Identify the blood parasite species.
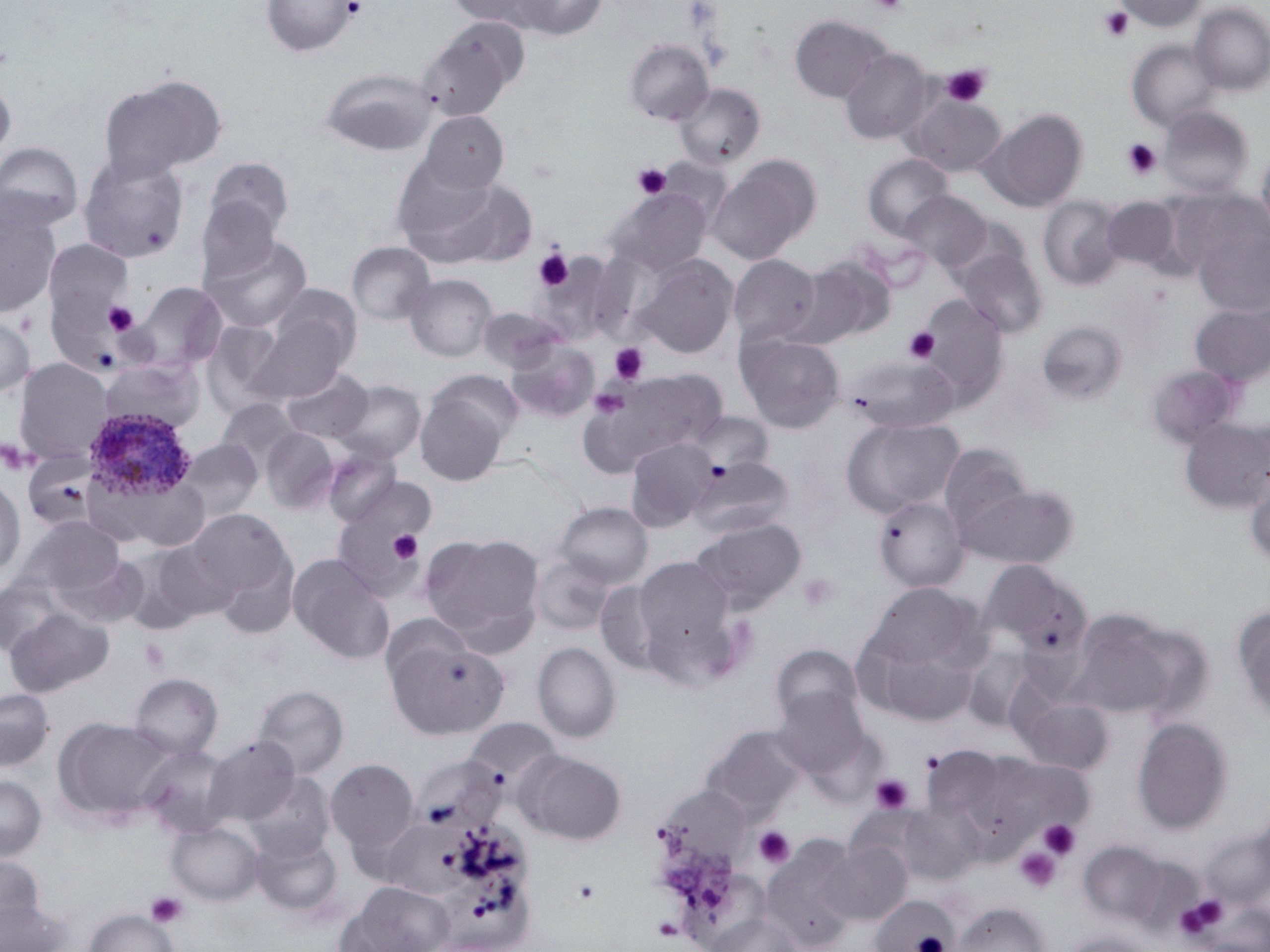
Plasmodium ovale.

{
  "modality": "optical microscopy",
  "platelet_locations": "approximate bounding boxes as (x1, y1, x2, y2) in pixels: (343, 0, 367, 19), (867, 0, 910, 14), (1097, 6, 1133, 43), (942, 64, 991, 108), (1121, 138, 1162, 179), (632, 162, 672, 200), (534, 248, 574, 291), (104, 301, 139, 336), (903, 326, 940, 364), (609, 342, 649, 384), (589, 387, 629, 419), (390, 531, 424, 563), (798, 572, 839, 613), (140, 639, 170, 672), (920, 751, 945, 774), (869, 774, 914, 815), (1039, 820, 1080, 859), (754, 826, 795, 869), (1014, 847, 1062, 893), (572, 877, 601, 905), (145, 891, 189, 928), (1178, 896, 1229, 936)",
  "field_of_view": "one of a larger specimen",
  "image_size": "1270×952 pixels",
  "uninfected_red_blood_cell_locations": "approximate bounding boxes as (x1, y1, x2, y2) in pixels: (260, 0, 360, 56), (510, 0, 607, 40), (1115, 0, 1206, 32), (445, 1, 551, 29), (1189, 2, 1270, 96), (788, 14, 892, 103), (419, 19, 529, 119), (624, 39, 714, 125), (1127, 39, 1220, 132), (838, 48, 933, 145), (320, 68, 437, 155), (98, 74, 226, 181), (0, 77, 16, 165), (673, 83, 765, 170), (903, 92, 1007, 176), (1158, 106, 1253, 197), (979, 108, 1088, 212), (418, 111, 509, 195), (0, 141, 84, 231), (1256, 149, 1270, 246), (78, 154, 189, 263), (862, 154, 954, 240), (707, 155, 821, 264), (202, 157, 294, 247), (391, 160, 525, 265), (606, 187, 713, 277), (195, 190, 286, 286), (898, 190, 992, 273), (1038, 196, 1125, 291), (1101, 196, 1180, 270), (0, 199, 61, 319), (1194, 226, 1270, 317), (203, 235, 312, 333), (44, 239, 134, 327), (347, 242, 435, 325), (953, 244, 1048, 338), (728, 254, 821, 346), (636, 255, 738, 358), (793, 255, 895, 346), (44, 270, 140, 380), (404, 274, 497, 361), (132, 282, 228, 373), (913, 294, 1009, 410), (244, 295, 359, 402), (1189, 303, 1270, 387), (477, 307, 566, 373), (0, 311, 36, 399), (1036, 319, 1129, 405), (203, 320, 290, 415), (736, 331, 846, 433), (505, 339, 599, 421), (849, 356, 958, 433), (13, 358, 114, 464), (1146, 364, 1242, 449), (281, 367, 374, 444), (99, 368, 203, 443), (587, 368, 729, 467), (333, 380, 426, 463), (414, 383, 512, 486), (216, 398, 301, 476), (1179, 417, 1270, 513), (842, 418, 964, 515), (260, 427, 340, 513), (625, 437, 717, 531), (179, 439, 263, 521), (939, 444, 1034, 537), (322, 445, 403, 526), (22, 452, 99, 532), (689, 455, 794, 538), (1244, 471, 1270, 568), (92, 472, 209, 553), (330, 474, 434, 599), (0, 477, 26, 579), (954, 482, 1079, 569), (872, 497, 967, 593), (553, 501, 653, 589), (184, 508, 295, 615), (13, 516, 127, 606), (691, 517, 806, 614), (419, 532, 545, 651), (208, 544, 301, 640), (114, 546, 204, 634), (55, 552, 148, 628), (287, 553, 394, 665), (531, 553, 617, 636), (629, 555, 739, 670), (979, 559, 1093, 661), (0, 578, 68, 657), (595, 579, 671, 676), (853, 585, 990, 724), (4, 606, 114, 697), (1233, 607, 1270, 723), (1066, 610, 1179, 720), (380, 613, 473, 690), (386, 637, 510, 739), (531, 642, 622, 743), (771, 644, 863, 728), (962, 646, 1039, 732), (129, 673, 223, 760), (253, 685, 349, 778), (772, 687, 873, 783), (0, 688, 54, 772), (1017, 695, 1113, 774), (52, 716, 175, 826), (1132, 717, 1233, 835), (464, 718, 562, 786), (701, 725, 807, 822), (204, 734, 301, 826), (139, 744, 234, 838), (517, 750, 626, 845), (325, 758, 419, 856), (415, 758, 510, 832), (243, 773, 335, 862), (0, 775, 47, 861), (654, 786, 753, 872), (897, 802, 985, 885), (166, 821, 264, 906), (391, 823, 472, 900), (1201, 831, 1269, 909), (250, 832, 342, 916), (759, 836, 861, 950), (820, 840, 911, 924), (1079, 841, 1169, 926), (0, 853, 45, 935), (340, 881, 455, 952), (870, 896, 958, 951), (0, 897, 68, 952), (954, 902, 1051, 952), (82, 908, 179, 952), (709, 913, 803, 952), (1063, 931, 1157, 952)",
  "magnification": "1000x",
  "preparation": "thin blood film",
  "stain": "May-Grünwald-Giemsa",
  "plasmodium_ovale_infected_red_blood_cell_locations": "approximate bounding boxes as (x1, y1, x2, y2) in pixels: (83, 407, 197, 504)"
}